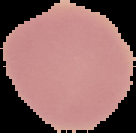 Segmented cell region on a black background. Image is 136×133 pixels. Malaria status: uninfected. From a thin blood film.